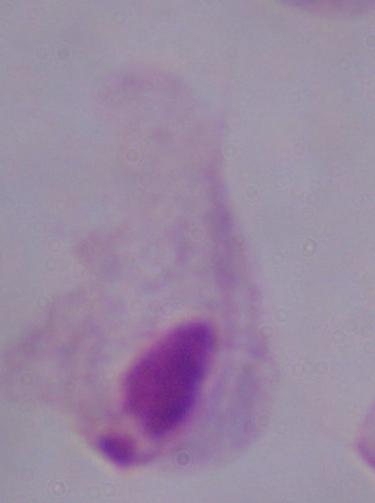
Photomicrograph. Captured at 1000x magnification. A trichomonad is shown.